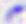

Summary:
  - Identification: Toxoplasma gondii
  - Modality: micrograph
  - Magnification: 400x